Identify the cell.
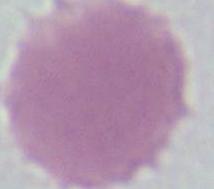

This is an erythrocyte.

modality = photomicrograph
magnification = 1000x